Comment on the morphology of the red blood cells.
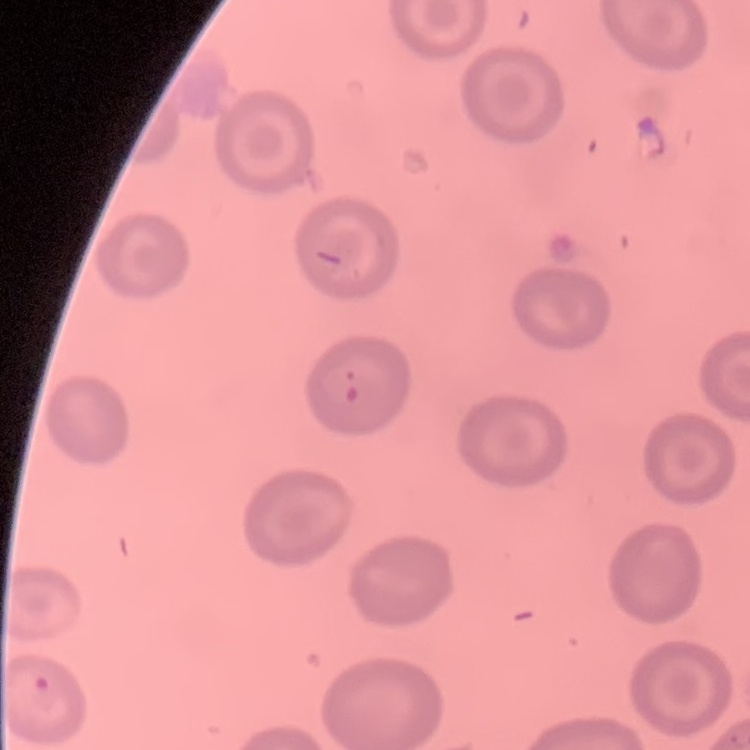
No rouleaux formation.

stain = Field's or Giemsa
preparation = thin blood film
image type = one tile cut from a larger photomicrograph